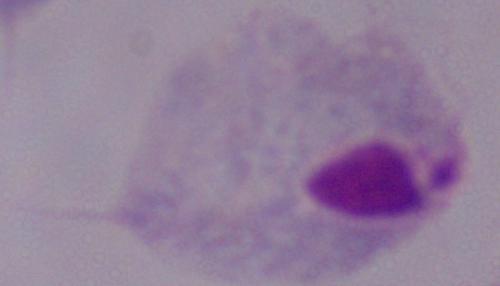

Photomicrograph. A trichomonad is seen. 1000x magnification.